Locate and identify every blood parasite.
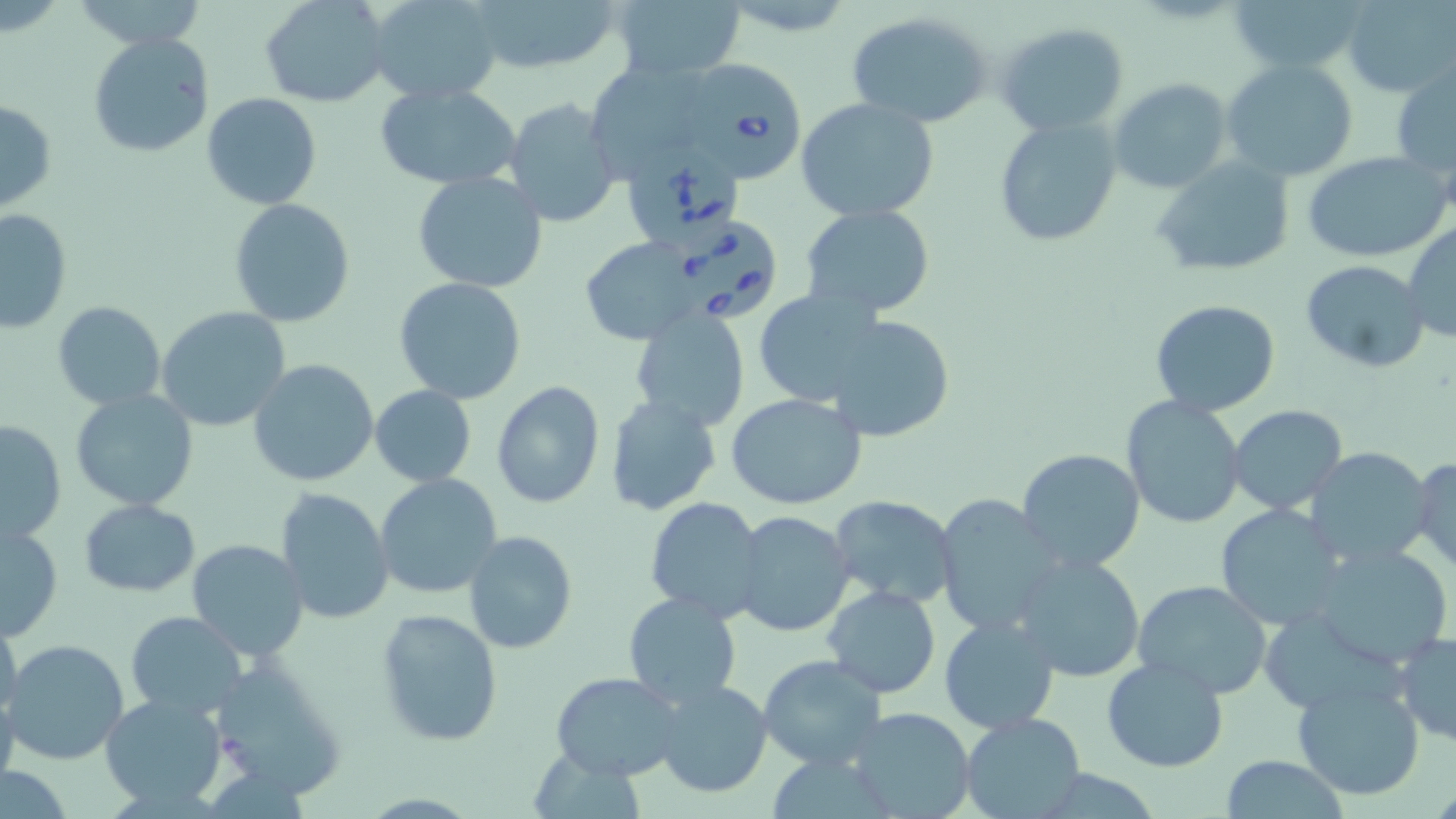
Approximate bounding boxes as named x1/y1/x2/y2 corners in pixels.
Babesia divergens-infected red blood cells: (x1=680, y1=64, x2=806, y2=184), (x1=624, y1=144, x2=749, y2=255), (x1=672, y1=224, x2=778, y2=321).
No Plasmodium falciparum, Plasmodium ovale, Plasmodium malariae, Plasmodium vivax, or Trypanosoma brucei observed.

Uninfected red blood cell locations: (x1=261, y1=0, x2=392, y2=108), (x1=366, y1=0, x2=505, y2=104), (x1=465, y1=0, x2=624, y2=78), (x1=612, y1=0, x2=748, y2=83), (x1=1228, y1=0, x2=1367, y2=76), (x1=1342, y1=0, x2=1455, y2=96), (x1=847, y1=10, x2=993, y2=127), (x1=995, y1=22, x2=1132, y2=136), (x1=87, y1=32, x2=215, y2=158), (x1=1222, y1=59, x2=1360, y2=184), (x1=1391, y1=64, x2=1456, y2=184), (x1=598, y1=67, x2=710, y2=179), (x1=1110, y1=78, x2=1234, y2=195), (x1=374, y1=82, x2=523, y2=189), (x1=202, y1=92, x2=323, y2=210), (x1=793, y1=96, x2=940, y2=224), (x1=503, y1=97, x2=622, y2=227), (x1=0, y1=99, x2=56, y2=214), (x1=995, y1=117, x2=1122, y2=247), (x1=1302, y1=149, x2=1450, y2=264), (x1=1150, y1=158, x2=1298, y2=277), (x1=411, y1=171, x2=547, y2=293), (x1=227, y1=198, x2=357, y2=328), (x1=798, y1=204, x2=936, y2=316), (x1=1, y1=208, x2=71, y2=334), (x1=1403, y1=221, x2=1456, y2=343), (x1=577, y1=237, x2=699, y2=344), (x1=1301, y1=258, x2=1430, y2=372), (x1=394, y1=276, x2=527, y2=406), (x1=752, y1=289, x2=887, y2=407), (x1=1150, y1=300, x2=1282, y2=417), (x1=52, y1=301, x2=166, y2=410), (x1=156, y1=306, x2=292, y2=431), (x1=630, y1=308, x2=753, y2=434), (x1=822, y1=312, x2=958, y2=444), (x1=249, y1=359, x2=379, y2=487), (x1=490, y1=380, x2=606, y2=510), (x1=369, y1=385, x2=477, y2=486), (x1=69, y1=387, x2=200, y2=513), (x1=727, y1=393, x2=867, y2=510), (x1=1121, y1=396, x2=1246, y2=529), (x1=605, y1=397, x2=720, y2=516), (x1=1228, y1=404, x2=1349, y2=515), (x1=1, y1=418, x2=68, y2=543), (x1=1304, y1=447, x2=1437, y2=570), (x1=1016, y1=448, x2=1145, y2=573), (x1=1411, y1=453, x2=1456, y2=574), (x1=374, y1=473, x2=504, y2=598), (x1=276, y1=488, x2=394, y2=625), (x1=934, y1=494, x2=1065, y2=639), (x1=645, y1=496, x2=766, y2=621), (x1=827, y1=496, x2=959, y2=609), (x1=78, y1=498, x2=201, y2=597), (x1=1214, y1=504, x2=1350, y2=632), (x1=731, y1=510, x2=856, y2=637), (x1=1, y1=521, x2=64, y2=640), (x1=463, y1=530, x2=577, y2=655), (x1=187, y1=539, x2=307, y2=662), (x1=1309, y1=541, x2=1455, y2=669), (x1=1014, y1=552, x2=1144, y2=682), (x1=1133, y1=580, x2=1276, y2=699), (x1=823, y1=586, x2=941, y2=698), (x1=623, y1=592, x2=743, y2=709), (x1=374, y1=607, x2=504, y2=748), (x1=0, y1=608, x2=23, y2=721), (x1=124, y1=611, x2=249, y2=719), (x1=939, y1=615, x2=1062, y2=735), (x1=1393, y1=631, x2=1456, y2=745), (x1=3, y1=639, x2=131, y2=766), (x1=203, y1=649, x2=348, y2=800), (x1=759, y1=655, x2=887, y2=771), (x1=1101, y1=657, x2=1230, y2=773), (x1=651, y1=667, x2=882, y2=786), (x1=551, y1=672, x2=683, y2=780), (x1=652, y1=678, x2=773, y2=799), (x1=1291, y1=678, x2=1425, y2=801), (x1=0, y1=691, x2=20, y2=797), (x1=99, y1=691, x2=228, y2=810), (x1=845, y1=707, x2=978, y2=819), (x1=959, y1=712, x2=1087, y2=819), (x1=1220, y1=756, x2=1350, y2=818). Slide-level diagnosis: Babesia divergens. Single field of view. May-Grünwald-Giemsa stain. Image is 1456×819 pixels. Thin blood film. 1000x magnification. Optical microscopy.